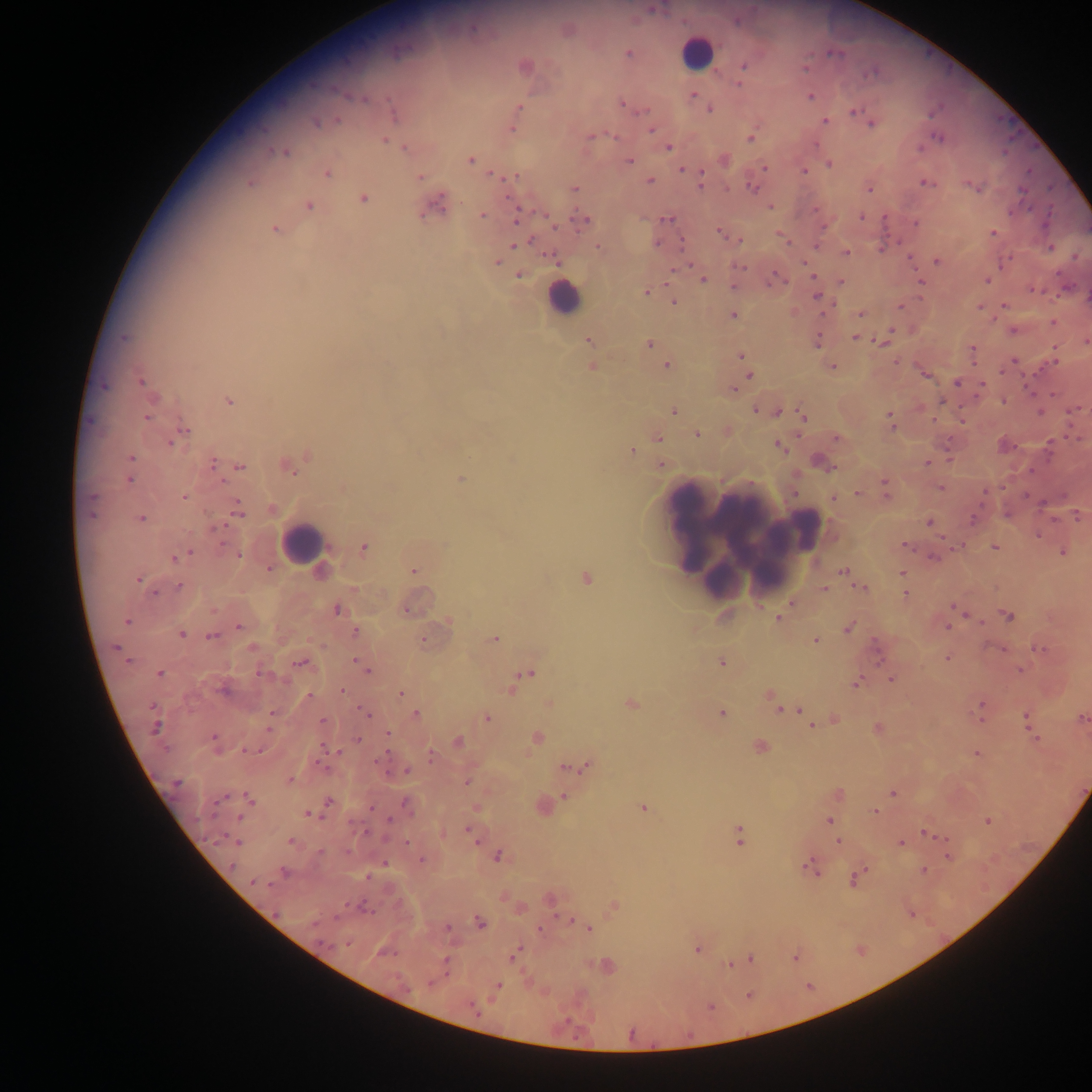
Approximate centers as x y in pixels.
Summary:
  - Leukocyte locations: 696 52; 562 298; 692 527; 807 528; 702 532; 744 537; 302 543
  - Malaria parasite locations: 654 10; 628 54; 743 66; 738 83; 692 95; 810 97; 363 99; 622 104; 519 108; 710 110; 854 111; 394 113; 866 120; 337 121; 825 121; 316 123; 871 124; 512 129; 650 130; 590 136; 615 137; 937 137; 751 138; 385 141; 405 148; 668 148; 285 153; 470 160; 629 161; 829 164; 765 168; 682 170; 805 170; 327 174; 494 175; 700 175; 514 177; 421 178; 650 181; 250 183; 925 183; 700 184; 750 187; 976 188; 574 189; 869 189; 1023 190; 364 199; 438 205; 309 206; 770 207; 483 215; 516 217; 862 217; 667 219; 585 221; 915 224; 274 230; 720 233; 993 233; 682 241; 517 243; 526 243; 657 243; 816 246; 598 247; 1050 248; 846 253; 552 258; 937 261; 497 262; 1004 262; 806 264; 738 266; 519 275; 777 279; 702 280; 986 280; 841 281; 921 281; 734 287; 1033 290; 646 292; 817 296; 674 302; 900 307; 1005 307; 979 308; 861 313; 734 315; 1053 321; 1014 331; 856 338; 884 338; 817 340; 589 341; 1085 342; 649 344; 971 350; 1054 354; 741 356; 1013 361; 897 362; 667 365; 591 366; 832 367; 749 375; 926 375; 141 381; 957 382; 982 385; 733 389; 229 401; 1003 401; 755 410; 674 411; 1041 412; 778 413; 147 417; 804 417; 890 417; 182 431; 697 434; 178 436; 837 437; 658 438; 171 442; 779 447; 1048 449; 632 451; 308 455; 131 457; 213 462; 820 462; 927 463; 661 465; 240 467; 289 468; 130 479; 460 479; 885 488; 940 488; 986 492; 857 494; 183 497; 833 499; 91 502; 238 509; 1077 516; 141 519; 973 520; 929 522; 905 545; 995 546; 363 548; 1063 552; 189 553; 238 555; 176 558; 934 558; 268 568; 414 570; 843 571; 902 573; 586 578; 138 580; 180 586; 863 588; 824 589; 154 593; 905 594; 956 608; 337 609; 407 612; 1008 616; 778 620; 126 622; 239 627; 947 627; 849 628; 355 632; 181 634; 212 636; 495 639; 815 641; 116 648; 252 648; 1039 648; 877 649; 947 658; 300 662; 358 662; 721 662; 365 669; 1019 670; 161 674; 261 674; 527 675; 892 679; 519 682; 857 683; 512 689; 224 690; 342 690; 400 693; 309 696; 771 697; 550 703; 631 704; 982 705; 782 708; 795 709; 721 713; 272 714; 367 714; 416 714; 1026 717; 487 718; 1082 719; 835 720; 323 721; 811 725; 155 727; 1029 727; 270 728; 878 728; 388 734; 213 738; 537 738; 359 739; 1036 739; 458 741; 760 747; 251 751; 976 753; 431 755; 322 765; 588 767; 570 768; 406 771; 290 780; 176 783; 466 783; 894 792; 838 795; 564 798; 222 799; 249 799; 329 801; 406 804; 644 808; 875 812; 309 814; 240 818; 389 818; 828 821; 988 821; 471 834; 927 834; 739 836; 233 840; 290 840; 838 840; 406 841; 901 844; 320 852; 949 856; 498 857; 422 860; 232 866; 811 868; 924 871; 284 872; 855 877; 255 883; 614 906; 362 907; 479 922; 447 927; 539 929; 589 929; 347 943; 698 949; 517 952; 795 957; 751 959; 446 963; 730 965; 432 982; 498 985; 472 1006
  - Field of view: single
  - Image size: 1092×1092 pixels
  - Preparation: thick blood smear
  - Capture: mobile-phone photograph through a microscope
  - Country: Ghana